Report the malaria status of this cell.
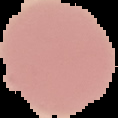

Uninfected.

From a thin blood film. Image is 118×118 pixels. Segmented cell region on a black background.